Report the malaria status of this cell.
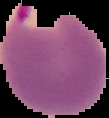
It is parasitized.

preparation = thin blood smear
image size = 109×118 pixels
image type = segmented cell region with the area outside set to black